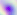

Photomicrograph. Toxoplasma gondii is shown. 400x magnification.